Report the malaria status of this cell.
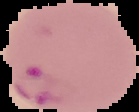

Parasitized.

image size = 139×112 pixels
preparation = thin blood smear
image type = cell region segmented out of the field of view; surrounding area masked to black